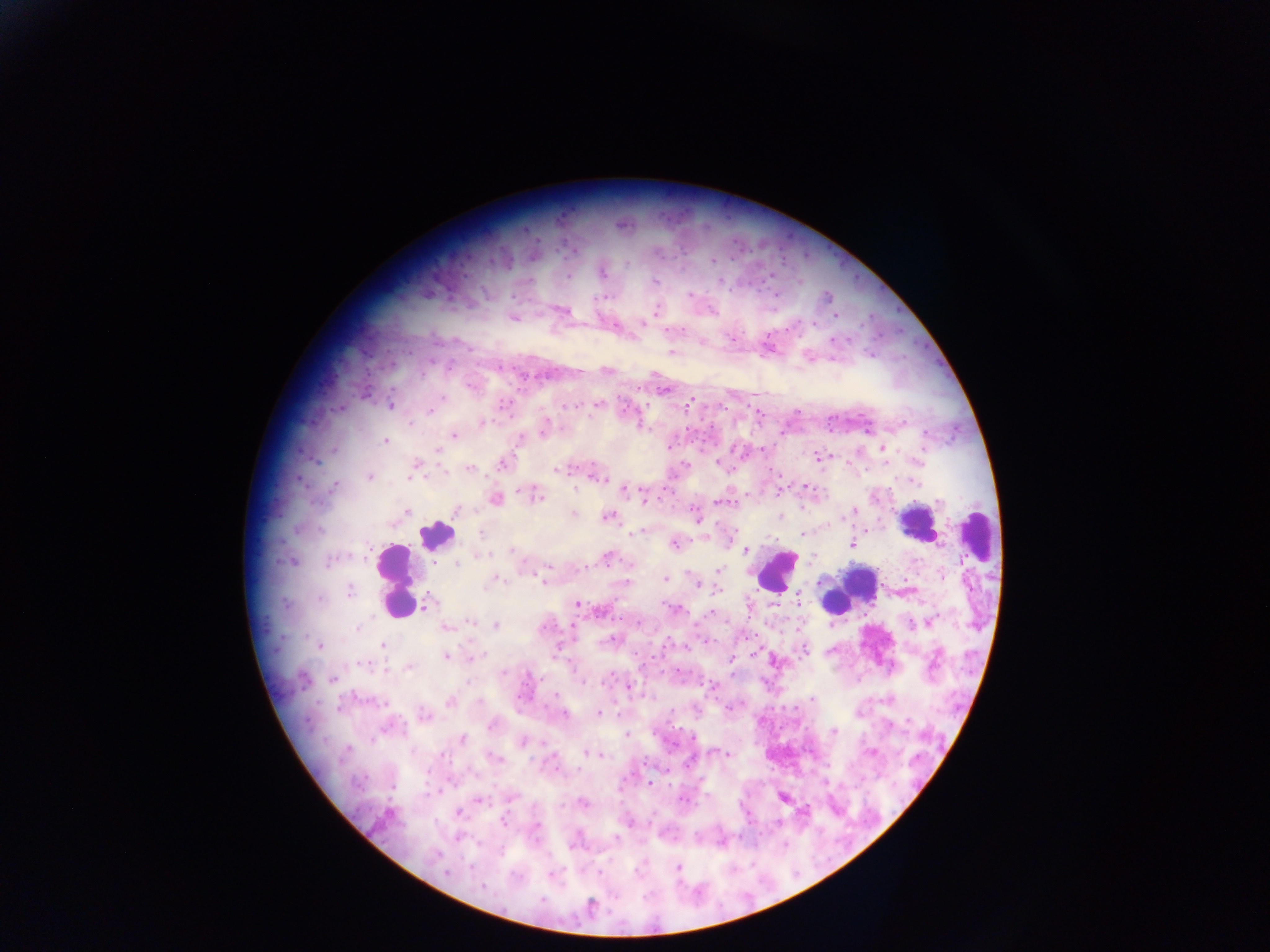
{
  "preparation": "thick blood smear",
  "capture": "mobile-phone photograph through a microscope",
  "image_size": "1270×952 pixels",
  "malaria_parasite_locations": "approximate centers as x y in pixels: 712 260; 626 263; 604 272; 568 276; 655 281; 690 294; 827 296; 561 310; 656 310; 513 318; 615 327; 833 340; 703 342; 671 352; 869 355; 606 370; 471 387; 662 390; 442 398; 691 400; 390 405; 565 405; 597 405; 430 411; 483 422; 409 423; 545 427; 453 436; 521 439; 386 442; 883 448; 438 451; 819 458; 717 463; 416 464; 502 464; 469 468; 556 470; 410 476; 597 476; 369 477; 913 481; 335 485; 806 486; 624 489; 535 496; 495 499; 721 502; 457 511; 407 512; 851 512; 574 514; 608 517; 780 517; 697 518; 320 530; 640 531; 481 533; 802 533; 674 543; 852 544; 745 549; 513 551; 483 554; 607 556; 329 561; 291 562; 457 563; 719 570; 943 576; 540 578; 665 579; 493 581; 696 582; 487 584; 717 590; 349 591; 799 600; 427 604; 577 604; 673 608; 710 613; 471 622; 928 622; 911 623; 495 626; 446 627; 357 628; 612 639; 383 645; 320 646; 804 650; 447 657; 475 657; 731 660; 363 665; 409 667; 503 673; 333 679; 608 679; 582 682; 709 685; 630 686; 812 699; 449 701; 598 713; 563 714; 425 716; 492 726; 834 731; 626 735; 462 739; 523 742; 346 750; 588 753; 870 753; 599 754; 727 755; 494 758; 650 783; 479 800; 683 800; 582 802; 459 813; 503 821; 538 827; 677 867; 599 872; 446 873; 551 873; 481 887; 590 905",
  "field_of_view": "single",
  "leukocyte_locations": "approximate centers as x y in pixels: 915 522; 976 532; 435 534; 776 571; 394 580; 850 591",
  "country": "Ghana"
}